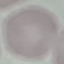
Summary:
  - Malaria status: uninfected
  - Preparation: thin smear
  - Stain: Giemsa
  - Capture: smartphone through the microscope eyepiece
  - Image type: cell patch, automatically extracted from a larger field of view and resized to 64 × 64 pixels